Give the extent of all uninfected red blood cells.
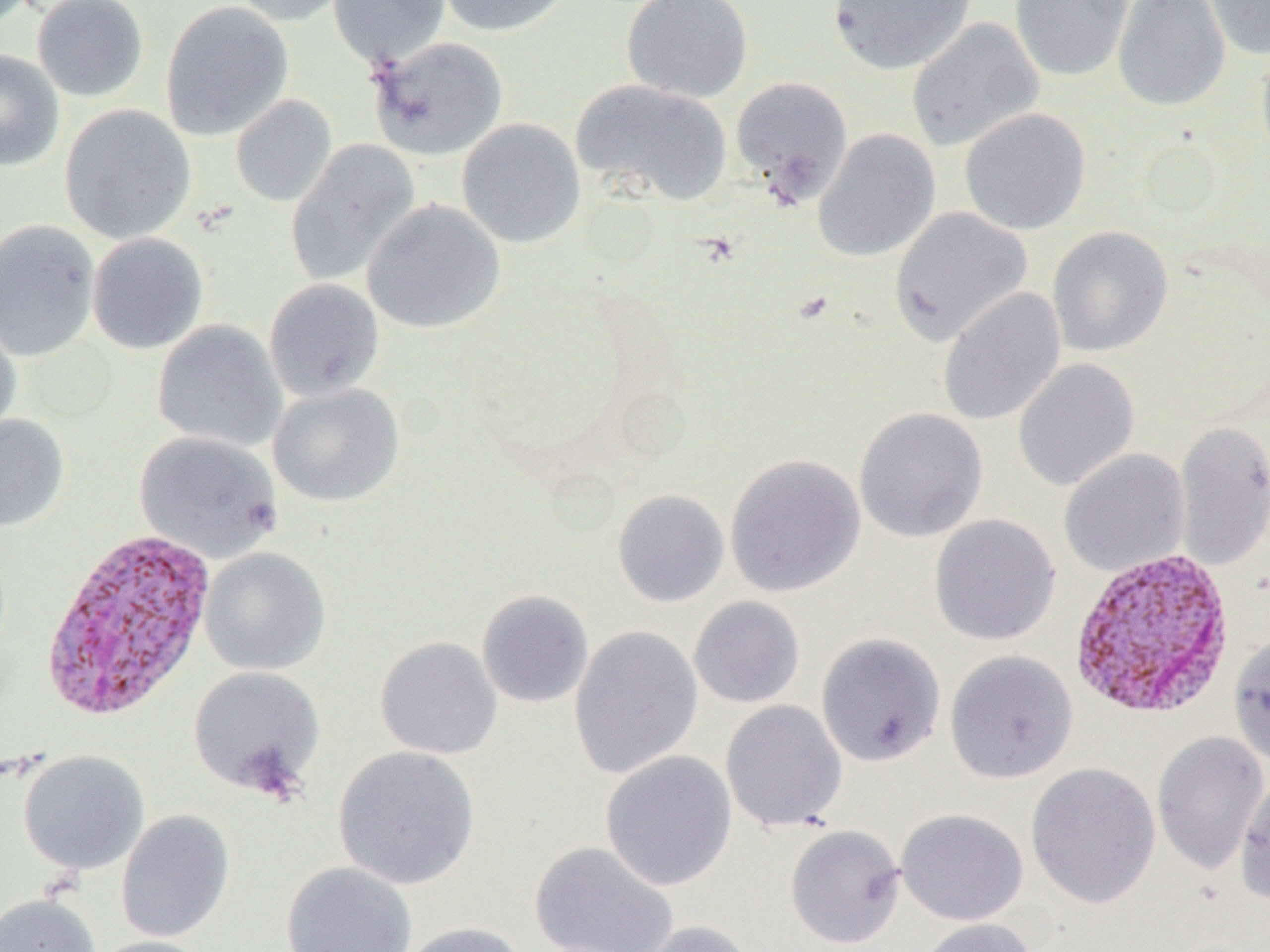
Approximate bounding boxes as named x1/y1/x2/y2 corners in pixels.
Uninfected red blood cells: (x1=32, y1=0, x2=149, y2=102), (x1=227, y1=0, x2=354, y2=27), (x1=328, y1=0, x2=451, y2=67), (x1=435, y1=0, x2=575, y2=37), (x1=621, y1=0, x2=754, y2=104), (x1=827, y1=0, x2=976, y2=75), (x1=1009, y1=0, x2=1134, y2=82), (x1=1112, y1=0, x2=1231, y2=112), (x1=1203, y1=0, x2=1270, y2=60), (x1=160, y1=1, x2=294, y2=141), (x1=906, y1=17, x2=1044, y2=152), (x1=368, y1=36, x2=509, y2=161), (x1=1255, y1=36, x2=1270, y2=166), (x1=0, y1=49, x2=65, y2=171), (x1=730, y1=76, x2=854, y2=205), (x1=571, y1=79, x2=733, y2=208), (x1=230, y1=94, x2=338, y2=207), (x1=59, y1=104, x2=197, y2=244), (x1=959, y1=107, x2=1091, y2=235), (x1=456, y1=118, x2=586, y2=249), (x1=813, y1=128, x2=941, y2=262), (x1=285, y1=140, x2=421, y2=287), (x1=362, y1=199, x2=506, y2=335), (x1=889, y1=207, x2=1033, y2=346), (x1=0, y1=219, x2=101, y2=362), (x1=1047, y1=226, x2=1174, y2=357), (x1=87, y1=232, x2=209, y2=354), (x1=263, y1=278, x2=385, y2=402), (x1=937, y1=286, x2=1067, y2=427), (x1=0, y1=314, x2=22, y2=444), (x1=152, y1=320, x2=287, y2=453), (x1=1012, y1=358, x2=1140, y2=491), (x1=267, y1=382, x2=405, y2=507), (x1=854, y1=407, x2=989, y2=542), (x1=0, y1=414, x2=70, y2=532), (x1=1173, y1=421, x2=1270, y2=570), (x1=135, y1=431, x2=283, y2=563), (x1=1058, y1=449, x2=1190, y2=576), (x1=725, y1=454, x2=866, y2=597), (x1=612, y1=489, x2=729, y2=607), (x1=929, y1=514, x2=1061, y2=646), (x1=200, y1=548, x2=331, y2=676), (x1=476, y1=589, x2=595, y2=708), (x1=688, y1=596, x2=805, y2=709), (x1=569, y1=625, x2=703, y2=779), (x1=816, y1=632, x2=946, y2=766), (x1=1228, y1=633, x2=1270, y2=766), (x1=374, y1=636, x2=502, y2=760), (x1=944, y1=649, x2=1078, y2=784), (x1=188, y1=666, x2=325, y2=795), (x1=721, y1=700, x2=847, y2=833), (x1=1151, y1=732, x2=1268, y2=874), (x1=333, y1=746, x2=480, y2=890), (x1=17, y1=749, x2=150, y2=876), (x1=600, y1=750, x2=737, y2=891), (x1=1026, y1=762, x2=1161, y2=908), (x1=1234, y1=774, x2=1270, y2=905), (x1=895, y1=808, x2=1028, y2=925), (x1=115, y1=810, x2=235, y2=943), (x1=784, y1=824, x2=906, y2=949), (x1=529, y1=841, x2=678, y2=952), (x1=281, y1=861, x2=417, y2=952), (x1=0, y1=893, x2=101, y2=952), (x1=913, y1=918, x2=1040, y2=952), (x1=634, y1=920, x2=758, y2=952), (x1=398, y1=921, x2=529, y2=952), (x1=89, y1=935, x2=218, y2=952).

Summary:
  - Plasmodium vivax-infected red blood cell locations: (x1=40, y1=527, x2=217, y2=722), (x1=1068, y1=547, x2=1237, y2=720)
  - Slide-level diagnosis: Plasmodium vivax
  - Image size: 1270×952 pixels
  - Magnification: 1000x
  - Preparation: thin blood smear
  - Field of view: single
  - Modality: light microscopy